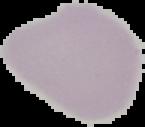

From a thin blood smear. Image is 145×127 pixels. Segmented cell region on a black background. Result: negative for malaria parasites.